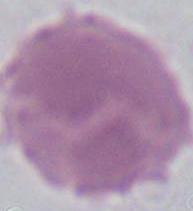
identification = red blood cell
modality = photomicrograph
magnification = 1000x